Name the parasite shown.
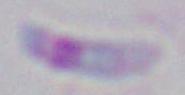

This is Toxoplasma gondii.

Summary:
  - Modality: micrograph
  - Magnification: 1000x